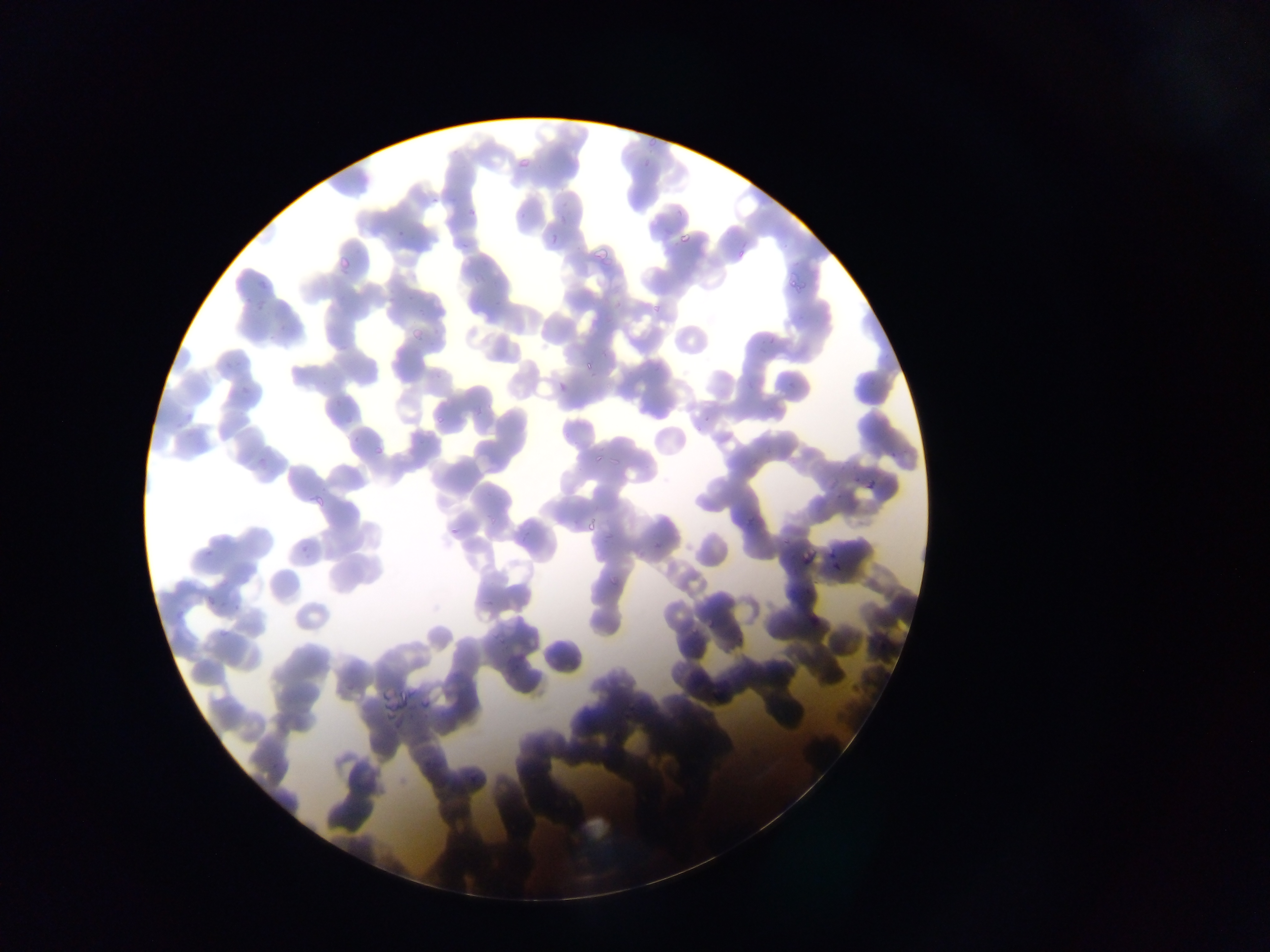
country = Ghana
capture = mobile-phone photograph through a microscope
malaria parasite locations = approximate bounding boxes as [left, top, right, bottom] in pixels: [646, 137, 659, 146], [517, 157, 530, 169], [466, 208, 477, 218], [549, 231, 557, 246], [680, 231, 692, 242], [462, 242, 472, 249], [591, 245, 610, 259], [738, 250, 745, 259], [339, 256, 351, 268], [788, 274, 800, 289], [798, 276, 810, 289], [258, 280, 268, 290], [651, 304, 665, 311], [411, 329, 424, 341], [225, 360, 232, 369], [584, 361, 592, 369], [241, 385, 251, 391], [436, 416, 444, 423], [374, 446, 382, 454], [595, 454, 600, 467], [609, 457, 623, 466], [313, 494, 325, 507], [746, 513, 754, 522], [588, 519, 595, 532], [450, 527, 459, 534], [802, 552, 810, 565], [608, 574, 618, 585], [209, 596, 216, 606], [220, 627, 229, 637], [382, 690, 390, 703], [395, 694, 407, 713], [420, 697, 434, 711], [379, 703, 395, 709], [386, 714, 395, 723] | approximate [x, y] pixel centers of objects too small to bound: [657, 546]
image size = 1270×952 pixels
preparation = thin blood smear
field of view = single